Give the extent of all uninfected red blood cells.
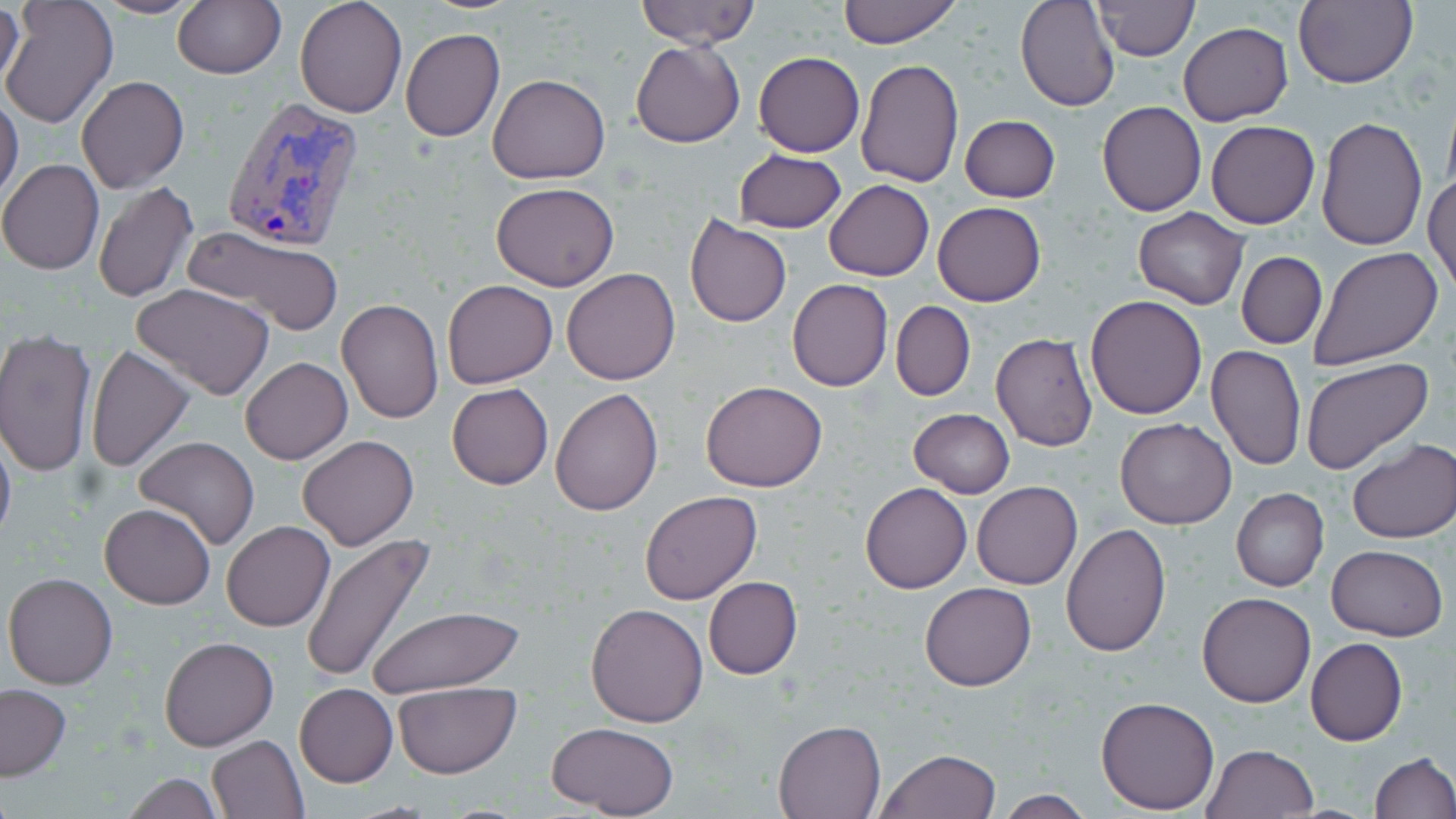

Approximate bounding boxes as (x1,y1)-(x2,y2) corner pairs in pixels.
Uninfected red blood cells: (93,0)-(203,19), (172,0)-(286,79), (295,0)-(406,119), (635,0)-(760,50), (837,0)-(961,47), (1015,0)-(1120,113), (1094,0)-(1198,60), (1295,0)-(1418,88), (0,2)-(118,130), (1,2)-(26,99), (1177,22)-(1292,127), (400,27)-(505,141), (631,42)-(745,148), (754,52)-(864,156), (856,57)-(964,188), (487,74)-(612,185), (76,76)-(189,192), (0,95)-(23,207), (1097,101)-(1206,217), (959,115)-(1060,203), (1316,116)-(1427,251), (1206,120)-(1320,229), (733,148)-(846,233), (0,159)-(104,275), (1425,175)-(1456,296), (92,180)-(198,304), (823,180)-(933,282), (490,181)-(620,291), (933,202)-(1045,306), (1133,208)-(1249,310), (684,215)-(791,328), (184,224)-(343,336), (1307,245)-(1444,371), (1236,252)-(1326,349), (562,268)-(681,385), (786,278)-(893,392), (442,280)-(558,388), (131,283)-(277,399), (1086,295)-(1207,420), (336,298)-(443,424), (892,301)-(975,401), (0,330)-(98,477), (990,331)-(1099,453), (86,343)-(193,472), (1206,345)-(1306,470), (241,357)-(352,464), (1302,358)-(1434,476), (702,381)-(827,493), (447,383)-(553,490), (550,387)-(665,517), (908,407)-(1014,497), (1114,417)-(1235,529), (0,431)-(16,551), (297,434)-(419,551), (134,437)-(259,550), (1346,438)-(1456,543), (971,481)-(1082,590), (860,482)-(972,594), (1231,488)-(1329,592), (640,491)-(761,604), (99,503)-(216,609), (221,520)-(335,632), (1062,523)-(1170,658), (302,534)-(434,685), (1326,544)-(1448,640), (3,571)-(118,690), (703,576)-(802,678), (919,581)-(1037,691), (1197,591)-(1315,708), (586,603)-(709,727), (367,605)-(521,696), (158,637)-(277,752), (1306,637)-(1407,746), (0,683)-(72,781), (294,684)-(398,787), (394,685)-(521,778), (1096,695)-(1221,813), (772,719)-(888,818), (544,721)-(679,817), (208,735)-(308,819), (1201,744)-(1320,819), (877,748)-(1001,818), (1371,751)-(1455,818), (119,772)-(222,818), (993,792)-(1098,818).

Summary:
  - Plasmodium vivax-infected red blood cell locations: (221,95)-(367,254)
  - Slide-level diagnosis: Plasmodium vivax
  - Modality: optical microscopy
  - Stain: May-Grünwald-Giemsa
  - Preparation: thin blood film
  - Field of view: single
  - Magnification: 1000x
  - Image size: 1456×819 pixels